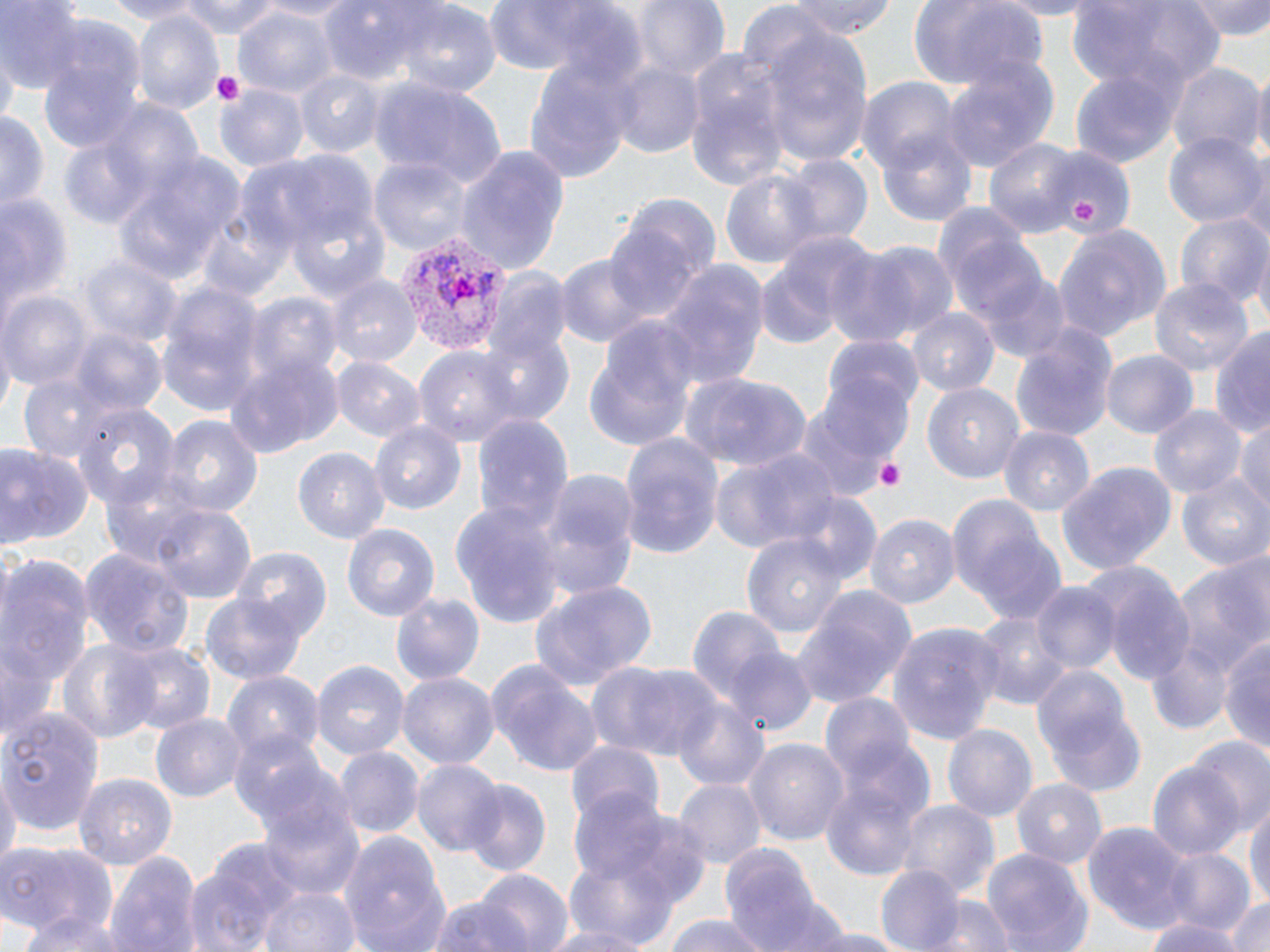

Summary:
  - Coordinate format: approximate bounding boxes as (x1, y1, x2, y2) in pixels
  - Platelet locations: (213, 68, 244, 105), (1071, 196, 1103, 224), (877, 458, 907, 492)
  - Uninfected red blood cell locations: (1, 0, 85, 92), (95, 0, 205, 23), (177, 0, 286, 39), (257, 0, 360, 21), (481, 0, 628, 74), (631, 0, 728, 84), (785, 0, 896, 39), (906, 0, 1048, 92), (986, 0, 1101, 16), (1067, 0, 1226, 94), (1191, 0, 1270, 40), (321, 1, 456, 90), (233, 5, 339, 100), (736, 5, 835, 76), (396, 6, 501, 98), (133, 9, 224, 116), (32, 28, 149, 156), (758, 29, 873, 169), (1, 49, 17, 132), (683, 50, 790, 189), (521, 54, 637, 188), (941, 60, 1060, 176), (1167, 60, 1263, 160), (609, 61, 706, 160), (295, 68, 384, 158), (1070, 68, 1180, 170), (1250, 68, 1270, 174), (371, 75, 507, 192), (856, 77, 962, 173), (214, 83, 307, 172), (0, 112, 48, 215), (877, 130, 976, 226), (55, 133, 159, 232), (1163, 133, 1265, 230), (984, 137, 1083, 234), (452, 144, 570, 275), (115, 147, 247, 286), (1042, 148, 1135, 239), (371, 154, 471, 256), (1240, 154, 1270, 254), (778, 155, 875, 249), (718, 167, 825, 273), (0, 188, 71, 328), (195, 198, 297, 302), (286, 200, 392, 302), (932, 201, 1040, 324), (603, 211, 707, 321), (1176, 214, 1267, 311), (1055, 221, 1171, 344), (754, 235, 874, 350), (860, 241, 960, 342), (819, 247, 924, 349), (555, 253, 654, 348), (77, 254, 179, 352), (655, 261, 769, 392), (974, 268, 1073, 364), (326, 271, 419, 366), (485, 273, 574, 372), (1150, 278, 1253, 382), (153, 283, 264, 416), (2, 292, 92, 389), (245, 294, 340, 388), (908, 309, 1000, 398), (578, 322, 700, 454), (1011, 324, 1119, 444), (1211, 326, 1270, 441), (64, 329, 167, 417), (473, 336, 574, 425), (818, 339, 921, 451), (226, 350, 342, 457), (415, 350, 520, 447), (1102, 350, 1198, 440), (331, 356, 423, 444), (680, 372, 811, 473), (19, 375, 117, 462), (799, 382, 911, 498), (924, 383, 1027, 482), (72, 399, 178, 505), (1150, 405, 1244, 500), (160, 413, 264, 519), (470, 414, 574, 534), (1233, 418, 1270, 517), (370, 422, 466, 516), (999, 425, 1098, 516), (619, 433, 724, 557), (0, 442, 93, 549), (293, 448, 390, 544), (708, 448, 842, 552), (1057, 460, 1176, 574), (531, 467, 641, 605), (1177, 471, 1269, 571), (948, 496, 1065, 627), (450, 501, 563, 626), (147, 502, 256, 607), (866, 513, 959, 607), (341, 523, 440, 619), (739, 528, 852, 641), (229, 545, 330, 643), (78, 546, 195, 655), (1, 551, 94, 701), (1170, 556, 1270, 699), (1089, 562, 1195, 684), (530, 579, 658, 694), (1032, 583, 1118, 674), (790, 585, 917, 708), (391, 592, 484, 687), (201, 593, 306, 685), (686, 608, 790, 711), (974, 612, 1076, 714), (887, 620, 1005, 743), (1147, 634, 1230, 733), (1218, 636, 1270, 755), (56, 637, 159, 745), (115, 641, 215, 739), (723, 647, 816, 738), (311, 658, 409, 760), (486, 658, 604, 775), (588, 660, 719, 762), (1029, 662, 1140, 784), (224, 671, 323, 760), (398, 671, 500, 770), (820, 695, 915, 791), (673, 698, 769, 790), (2, 703, 109, 836), (151, 713, 246, 803), (943, 723, 1039, 825), (229, 729, 333, 836), (745, 737, 848, 848), (1190, 738, 1270, 833), (565, 743, 664, 831), (334, 746, 423, 837), (412, 758, 505, 855), (1146, 761, 1244, 862), (0, 768, 18, 878), (74, 772, 178, 871), (674, 778, 765, 869), (821, 778, 922, 879), (1009, 778, 1106, 867), (460, 780, 551, 878), (569, 790, 682, 891), (255, 796, 366, 904), (1246, 798, 1270, 913), (897, 801, 998, 896), (1083, 822, 1193, 932), (340, 829, 450, 952), (0, 842, 118, 942), (183, 843, 304, 950), (723, 845, 822, 952), (981, 847, 1091, 952), (104, 848, 201, 952), (1160, 849, 1252, 934), (559, 853, 685, 947), (876, 865, 966, 951), (472, 867, 573, 952), (255, 883, 360, 952), (1222, 893, 1270, 952), (425, 896, 539, 952), (922, 896, 1015, 952), (763, 898, 855, 952), (13, 906, 134, 952), (663, 914, 772, 952), (1141, 915, 1247, 952), (531, 922, 661, 952), (795, 925, 909, 952)
  - Plasmodium vivax-infected red blood cell locations: (390, 230, 510, 353)
  - Slide-level diagnosis: Plasmodium vivax
  - Preparation: thin blood film
  - Magnification: 1000x
  - Stain: May-Grünwald-Giemsa
  - Modality: light microscopy
  - Image size: 1270×952 pixels
  - Field of view: single